Assess this cell for malaria.
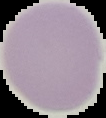
Uninfected.

preparation = thin blood film
image size = 106×118 pixels
image type = segmented cell region on a black background